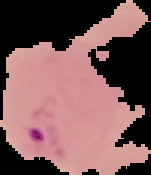
Malaria status: parasitized. From a thin blood film. Cell region segmented out of the field of view; the surrounding area is masked to black. Image is 151×175 pixels.